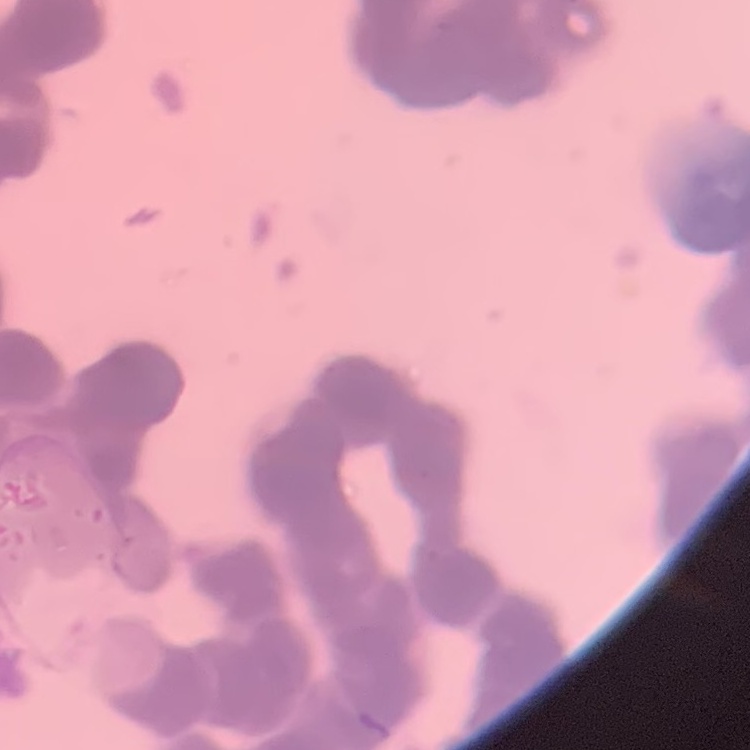
red blood cell morphology = rouleaux formation
stain = Field's or Giemsa
preparation = thin peripheral smear
image type = square crop of a larger photomicrograph